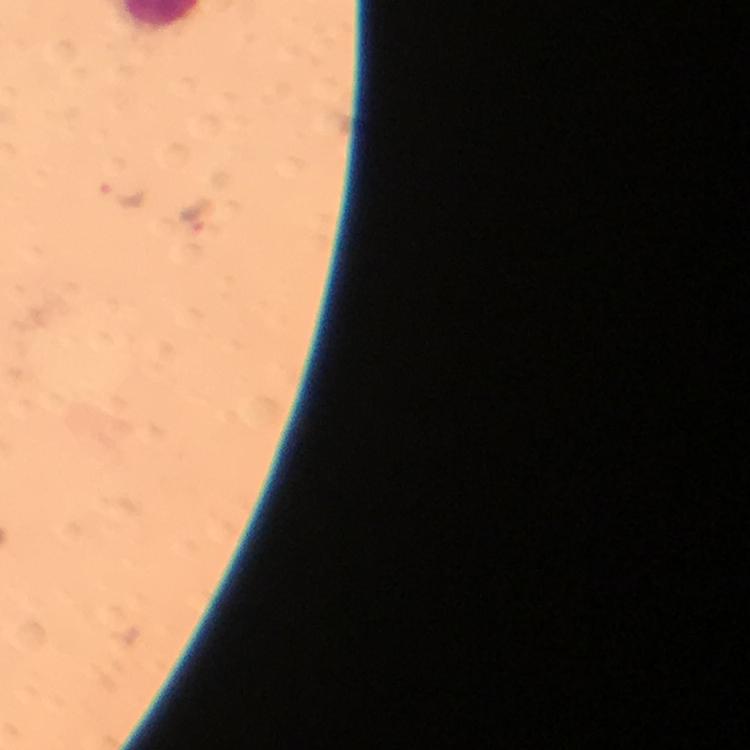
Approximate centers as {x, y} in pixels.
Summary:
  - Plasmodium parasite locations: {119, 196}, {196, 214}
  - Image size: 750×750 pixels
  - Cropped from: one field of view
  - Preparation: thick blood film
  - Capture: smartphone mounted on the microscope
  - Immersion oil: applied
  - Magnification: 100x
  - Context: from a malaria diagnostic workup
  - Stain: Giemsa